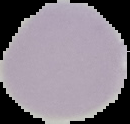
Summary:
  - Image type: segmented cell region with the area outside set to black
  - Image size: 130×124 pixels
  - Preparation: thin blood film
  - Result: negative for Plasmodium parasites